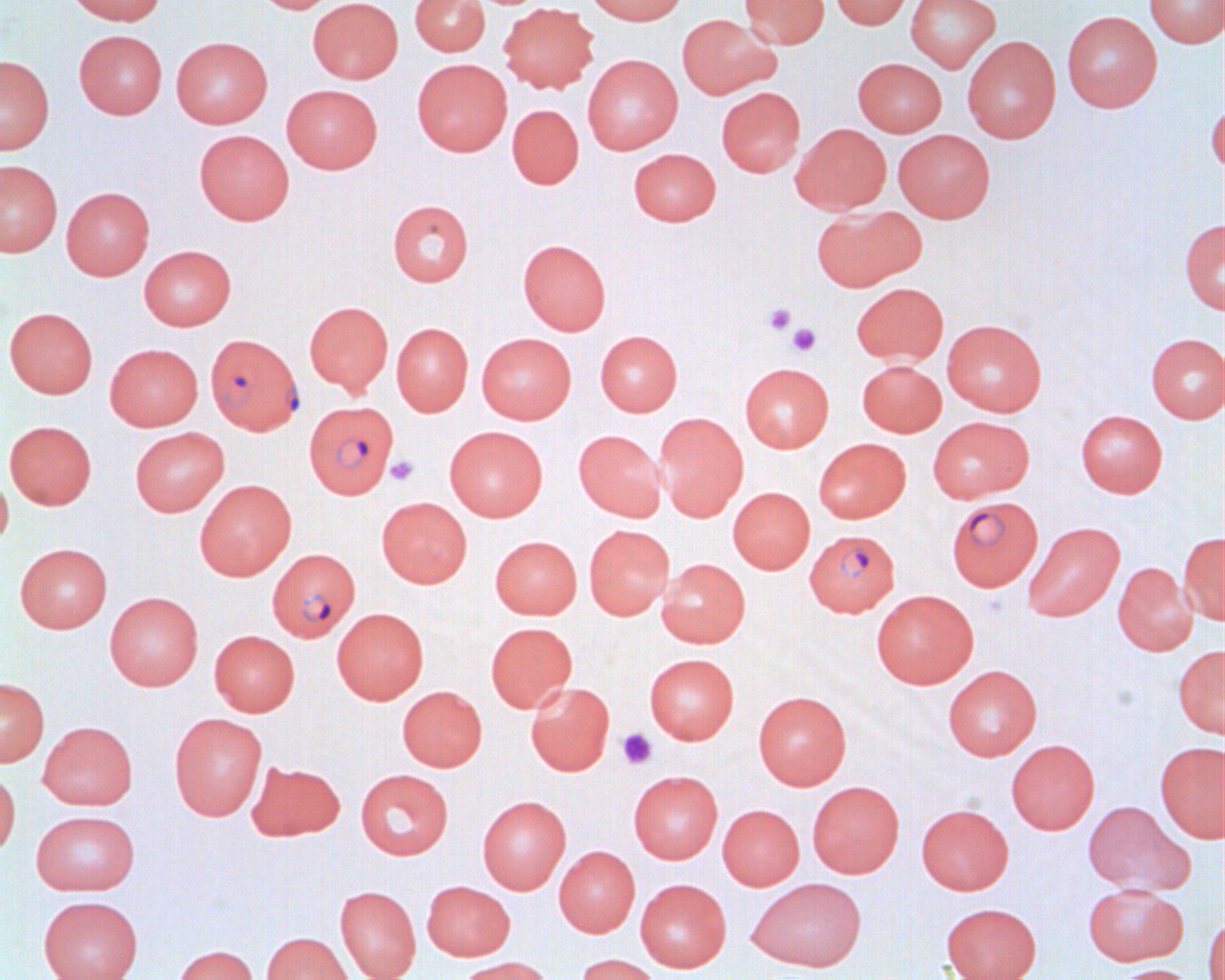
slide_level_diagnosis: Plasmodium falciparum
image_size: 1225×980 pixels
field_of_view: single
modality: optical microscopy
uninfected_red_blood_cell_locations: 'approximate bounding boxes as named x1/y1/x2/y2 corners in pixels: (x1=64, y1=0, x2=166, y2=25), (x1=255, y1=0, x2=338, y2=14), (x1=308, y1=0, x2=403, y2=84), (x1=410, y1=0, x2=489, y2=56), (x1=584, y1=0, x2=687, y2=25), (x1=740, y1=0, x2=829, y2=48), (x1=830, y1=0, x2=912, y2=29), (x1=905, y1=0, x2=1000, y2=72), (x1=1144, y1=0, x2=1224, y2=48), (x1=497, y1=2, x2=599, y2=94), (x1=1061, y1=10, x2=1162, y2=112), (x1=677, y1=13, x2=780, y2=99), (x1=74, y1=30, x2=167, y2=119), (x1=962, y1=35, x2=1061, y2=143), (x1=171, y1=36, x2=272, y2=128), (x1=583, y1=54, x2=683, y2=154), (x1=0, y1=55, x2=54, y2=154), (x1=853, y1=57, x2=946, y2=136), (x1=412, y1=58, x2=512, y2=156), (x1=282, y1=84, x2=383, y2=173), (x1=717, y1=87, x2=806, y2=177), (x1=1206, y1=98, x2=1224, y2=177), (x1=507, y1=104, x2=584, y2=189), (x1=791, y1=123, x2=891, y2=215), (x1=194, y1=129, x2=294, y2=225), (x1=893, y1=129, x2=995, y2=222), (x1=629, y1=148, x2=721, y2=226), (x1=0, y1=160, x2=62, y2=257), (x1=61, y1=187, x2=154, y2=280), (x1=388, y1=200, x2=473, y2=286), (x1=811, y1=206, x2=924, y2=291), (x1=1180, y1=219, x2=1225, y2=313), (x1=518, y1=239, x2=611, y2=335), (x1=139, y1=245, x2=236, y2=330), (x1=851, y1=282, x2=948, y2=365), (x1=304, y1=301, x2=393, y2=395), (x1=4, y1=307, x2=98, y2=398), (x1=942, y1=319, x2=1046, y2=416), (x1=391, y1=323, x2=473, y2=416), (x1=595, y1=330, x2=682, y2=415), (x1=476, y1=332, x2=576, y2=423), (x1=1145, y1=333, x2=1225, y2=423), (x1=105, y1=343, x2=203, y2=430), (x1=857, y1=360, x2=946, y2=436), (x1=740, y1=363, x2=833, y2=452), (x1=1075, y1=410, x2=1167, y2=498), (x1=653, y1=412, x2=748, y2=521), (x1=928, y1=416, x2=1033, y2=503), (x1=5, y1=420, x2=96, y2=509), (x1=444, y1=425, x2=547, y2=521), (x1=129, y1=427, x2=229, y2=516), (x1=573, y1=429, x2=666, y2=521), (x1=814, y1=438, x2=911, y2=523), (x1=0, y1=469, x2=13, y2=549), (x1=194, y1=479, x2=296, y2=581), (x1=727, y1=486, x2=814, y2=574), (x1=377, y1=497, x2=472, y2=587), (x1=1024, y1=522, x2=1123, y2=620), (x1=584, y1=524, x2=674, y2=619), (x1=1178, y1=532, x2=1225, y2=624), (x1=490, y1=536, x2=582, y2=619), (x1=15, y1=543, x2=112, y2=632), (x1=657, y1=558, x2=750, y2=648), (x1=1113, y1=562, x2=1198, y2=656), (x1=871, y1=589, x2=978, y2=688), (x1=104, y1=591, x2=203, y2=690), (x1=332, y1=607, x2=428, y2=704), (x1=486, y1=622, x2=576, y2=712), (x1=209, y1=630, x2=299, y2=717), (x1=1174, y1=644, x2=1225, y2=739), (x1=644, y1=653, x2=739, y2=744), (x1=942, y1=665, x2=1042, y2=760), (x1=0, y1=677, x2=49, y2=766), (x1=525, y1=682, x2=614, y2=776), (x1=397, y1=686, x2=487, y2=771), (x1=753, y1=691, x2=851, y2=789), (x1=169, y1=712, x2=267, y2=820), (x1=38, y1=721, x2=137, y2=810), (x1=1006, y1=739, x2=1099, y2=834), (x1=1155, y1=741, x2=1225, y2=843), (x1=246, y1=761, x2=345, y2=840), (x1=0, y1=769, x2=20, y2=859), (x1=356, y1=769, x2=453, y2=859), (x1=628, y1=770, x2=723, y2=863), (x1=807, y1=781, x2=904, y2=878), (x1=478, y1=795, x2=571, y2=894), (x1=1082, y1=801, x2=1191, y2=894), (x1=718, y1=804, x2=804, y2=890), (x1=917, y1=804, x2=1013, y2=894), (x1=31, y1=810, x2=140, y2=895), (x1=554, y1=845, x2=640, y2=937), (x1=635, y1=878, x2=731, y2=972), (x1=748, y1=878, x2=867, y2=971), (x1=422, y1=881, x2=515, y2=960), (x1=1082, y1=883, x2=1188, y2=966), (x1=335, y1=885, x2=421, y2=980), (x1=38, y1=895, x2=143, y2=980), (x1=941, y1=902, x2=1042, y2=980), (x1=1203, y1=911, x2=1224, y2=980), (x1=262, y1=932, x2=353, y2=980), (x1=173, y1=944, x2=258, y2=980), (x1=575, y1=953, x2=662, y2=980), (x1=454, y1=956, x2=556, y2=980), (x1=1111, y1=964, x2=1198, y2=980)'
preparation: thin blood film
plasmodium_falciparum_infected_red_blood_cell_locations: 'approximate bounding boxes as named x1/y1/x2/y2 corners in pixels: (x1=209, y1=334, x2=306, y2=441), (x1=309, y1=404, x2=403, y2=502), (x1=946, y1=496, x2=1043, y2=591), (x1=805, y1=529, x2=899, y2=616), (x1=267, y1=548, x2=360, y2=642)'
magnification: 1000x
platelet_locations: 'approximate bounding boxes as named x1/y1/x2/y2 corners in pixels: (x1=763, y1=303, x2=796, y2=335), (x1=787, y1=323, x2=821, y2=356), (x1=386, y1=456, x2=418, y2=486), (x1=616, y1=728, x2=656, y2=770)'